Assess this cell for malaria.
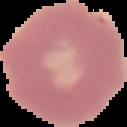

Uninfected.

Summary:
  - Preparation: thin blood film
  - Image size: 127×127 pixels
  - Image type: cell region segmented out of the field of view; surrounding area masked to black